Comment on the morphology of the erythrocytes.
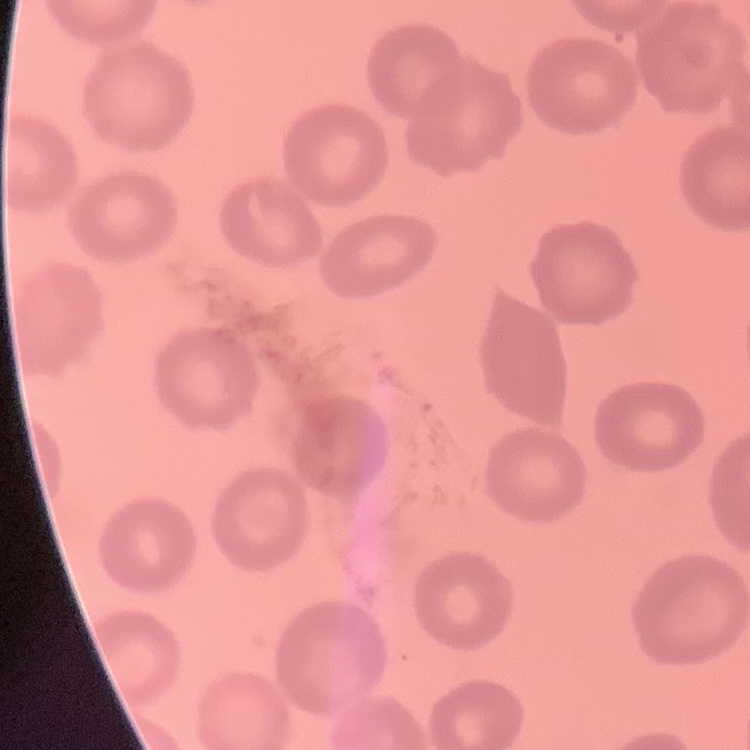

They show no rouleaux formation.

preparation = thin blood film
image type = one tile cut from a larger photomicrograph
stain = Field's or Giemsa